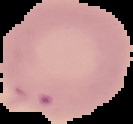

malaria status = uninfected
image type = segmented cell region with the area outside set to black
preparation = thin blood smear
image size = 133×124 pixels